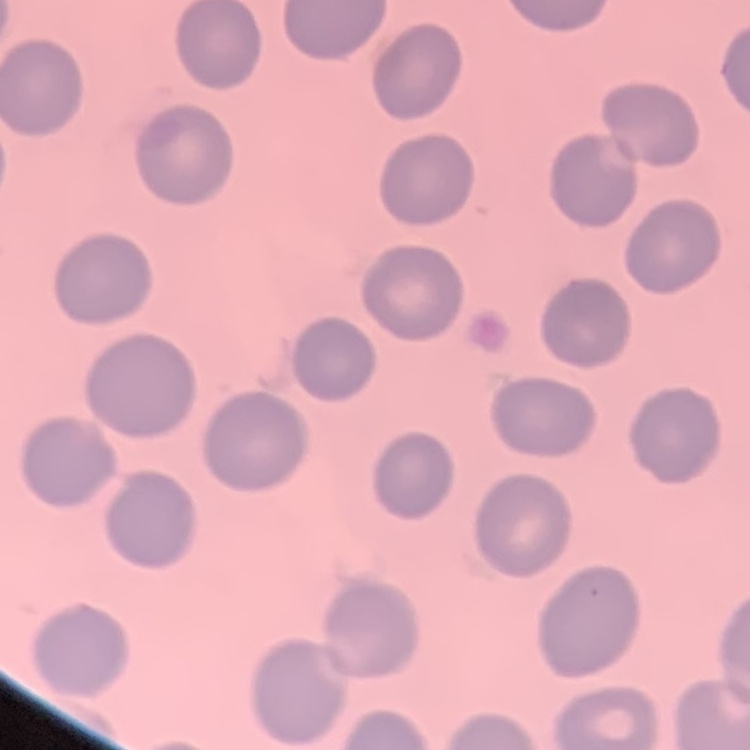

{
  "erythrocyte_morphology": "no rouleaux formation",
  "stain": "Field's or Giemsa",
  "image_type": "square crop of a larger photomicrograph",
  "preparation": "thin peripheral smear"
}